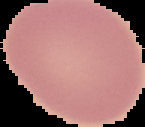

Summary:
  - Image type: cell region segmented out of the field of view; surrounding area masked to black
  - Image size: 145×127 pixels
  - Malaria status: uninfected
  - Preparation: thin blood film